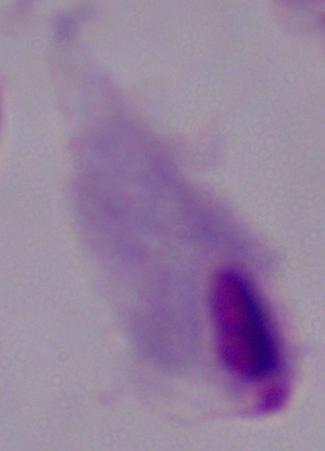

Photomicrograph. A trichomonad is seen. 1000x magnification.